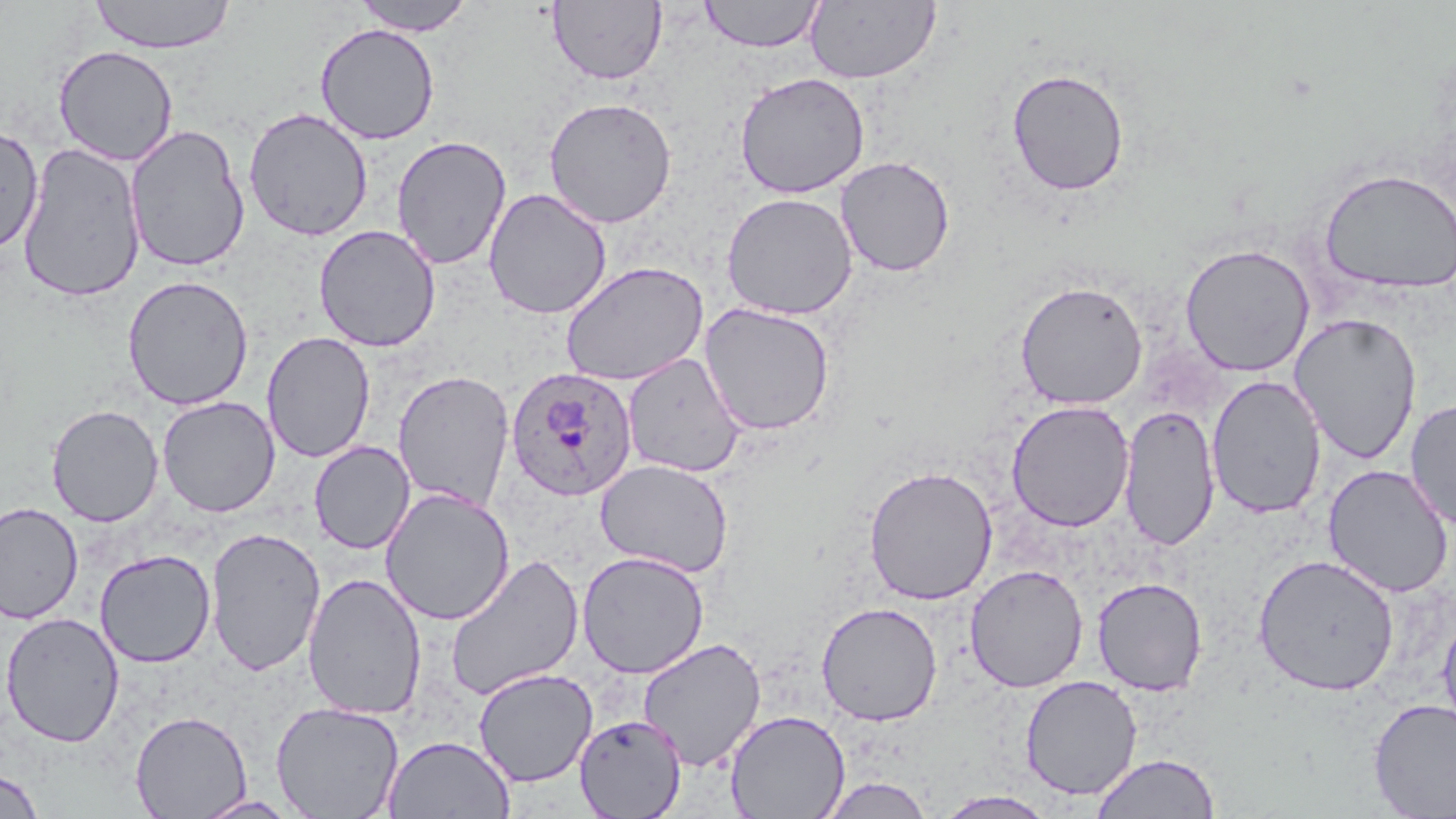
{
  "slide_level_diagnosis": "Plasmodium ovale",
  "stain": "May-Grünwald-Giemsa",
  "uninfected_red_blood_cell_locations": "approximate bounding boxes as (x1, y1, x2, y2) in pixels: (88, 0, 236, 54), (351, 0, 476, 36), (699, 0, 825, 53), (547, 1, 668, 85), (805, 1, 941, 84), (314, 23, 440, 145), (53, 45, 179, 165), (1006, 68, 1129, 196), (734, 71, 870, 199), (543, 96, 677, 229), (243, 106, 373, 241), (125, 123, 250, 272), (0, 124, 44, 255), (391, 135, 511, 270), (17, 142, 146, 303), (835, 155, 956, 277), (1319, 167, 1456, 294), (483, 188, 612, 319), (721, 192, 858, 320), (314, 224, 441, 352), (1179, 243, 1315, 376), (560, 260, 709, 386), (121, 275, 254, 410), (1015, 280, 1148, 410), (699, 302, 836, 436), (1289, 312, 1423, 465), (261, 331, 375, 463), (622, 353, 745, 478), (392, 370, 515, 511), (1207, 375, 1326, 519), (157, 396, 280, 517), (1405, 397, 1456, 531), (1006, 400, 1134, 532), (46, 404, 164, 527), (1119, 404, 1220, 552), (310, 441, 415, 554), (595, 459, 734, 578), (863, 465, 998, 604), (1323, 465, 1453, 597), (380, 488, 515, 626), (0, 502, 83, 624), (324, 522, 450, 674), (205, 526, 326, 676), (94, 549, 216, 668), (576, 550, 710, 679), (445, 553, 585, 701), (1253, 553, 1400, 695), (965, 564, 1088, 693), (303, 572, 427, 721), (1092, 577, 1208, 696), (816, 602, 943, 726), (1437, 603, 1456, 746), (1, 612, 125, 748), (638, 637, 766, 771), (473, 668, 597, 787), (1020, 675, 1142, 800), (1369, 698, 1456, 819), (271, 700, 405, 819), (725, 709, 850, 818), (130, 710, 252, 819), (574, 714, 687, 819), (383, 735, 515, 819), (1091, 753, 1221, 819), (0, 768, 44, 818), (818, 776, 936, 818), (935, 790, 1058, 818), (193, 795, 300, 819)",
  "magnification": "1000x",
  "image_size": "1456×819 pixels",
  "preparation": "thin blood film",
  "field_of_view": "one of a larger specimen",
  "modality": "light microscopy",
  "plasmodium_ovale_infected_red_blood_cell_locations": "approximate bounding boxes as (x1, y1, x2, y2) in pixels: (506, 367, 637, 502)"
}